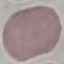

malaria status = uninfected
preparation = thin blood smear
capture = smartphone camera at the microscope eyepiece
image type = automatically extracted cell patch, resized to 64 × 64 pixels
stain = Giemsa